Locate every Plasmodium falciparum-infected red blood cell.
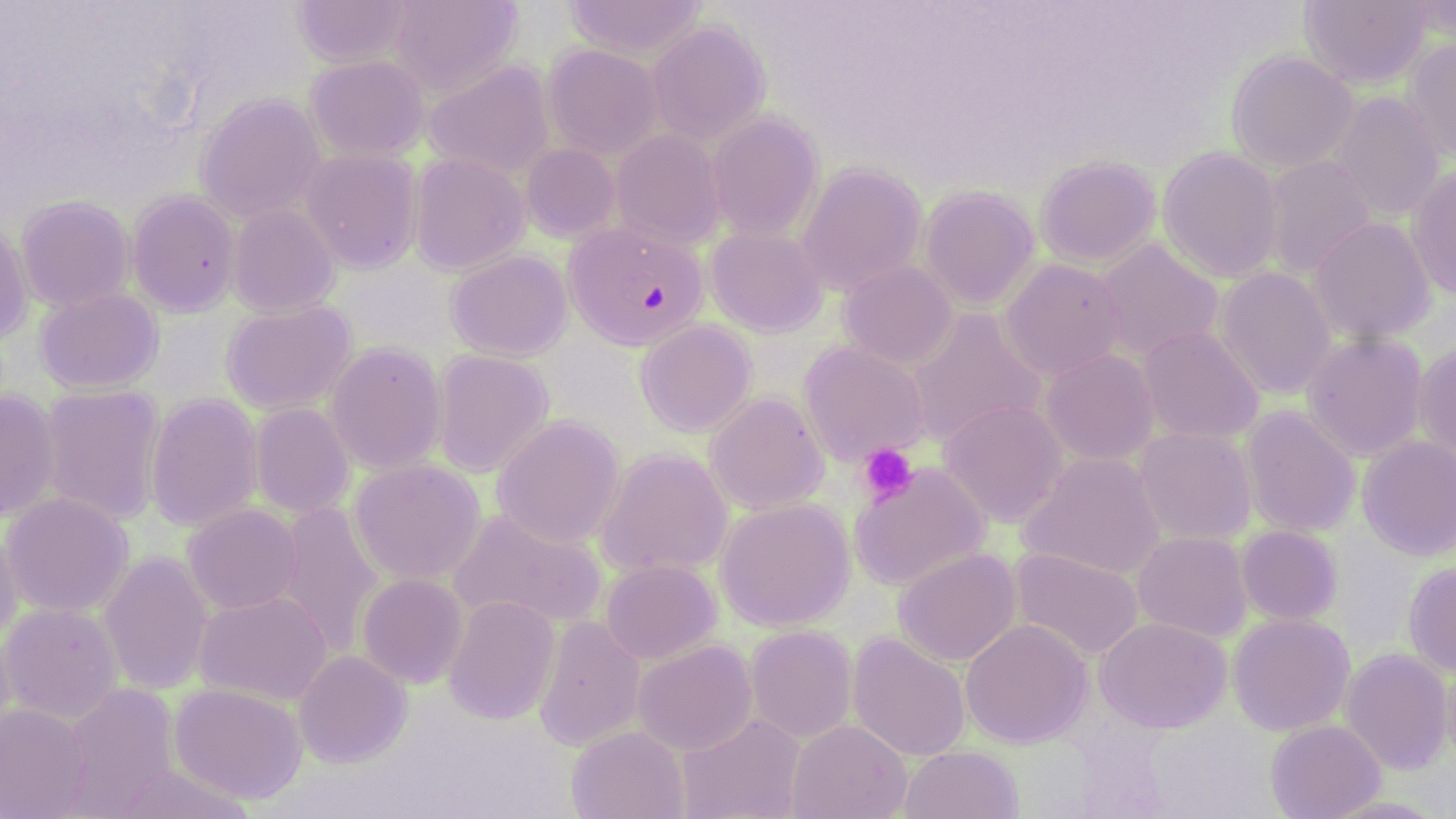
Approximate bounding boxes as (x1,y1)-(x2,y2) corner pairs in pixels.
Plasmodium falciparum-infected red blood cells: (564,221)-(708,350).

Summary:
  - Uninfected red blood cell locations: (387,0)-(522,96), (564,0)-(707,60), (1299,0)-(1430,89), (292,1)-(416,67), (1403,1)-(1455,41), (647,20)-(770,146), (1404,36)-(1456,162), (542,44)-(663,160), (1226,51)-(1358,171), (305,55)-(430,161), (423,61)-(556,181), (1329,91)-(1444,222), (195,93)-(325,223), (707,112)-(823,242), (611,130)-(726,249), (521,143)-(620,242), (1157,146)-(1283,283), (301,149)-(423,273), (410,153)-(529,275), (1262,155)-(1376,278), (1034,156)-(1161,268), (796,163)-(927,295), (1407,166)-(1456,299), (919,186)-(1039,310), (127,191)-(241,316), (16,195)-(135,311), (228,204)-(340,318), (1308,216)-(1436,344), (0,221)-(33,345), (705,226)-(828,337), (1094,239)-(1224,361), (446,249)-(572,360), (999,258)-(1127,382), (838,261)-(958,369), (1215,267)-(1336,400), (35,288)-(163,394), (220,301)-(356,414), (906,308)-(1047,447), (635,319)-(757,437), (1137,325)-(1264,444), (1302,332)-(1428,461), (325,342)-(447,475), (799,342)-(931,466), (1413,342)-(1456,467), (432,349)-(554,478), (1041,349)-(1159,465), (40,384)-(166,525), (0,389)-(61,523), (145,393)-(263,532), (705,393)-(829,514), (938,400)-(1068,527), (250,403)-(354,519), (1240,406)-(1360,537), (492,415)-(625,548), (1134,427)-(1256,545), (1356,435)-(1456,561), (596,447)-(733,578), (1019,452)-(1166,580), (348,459)-(486,584), (849,462)-(990,591), (1,492)-(135,618), (715,498)-(855,631), (275,501)-(384,656), (182,504)-(302,614), (447,509)-(608,632), (0,523)-(21,643), (1237,525)-(1343,625), (1133,531)-(1252,641), (1009,547)-(1143,660), (894,548)-(1021,666), (99,551)-(213,696), (600,559)-(721,664), (1403,562)-(1456,676), (357,573)-(468,688), (193,591)-(332,706), (443,595)-(560,725), (0,603)-(124,724), (1227,613)-(1355,736), (533,615)-(646,750), (1095,617)-(1232,733), (960,619)-(1092,748), (745,625)-(857,744), (0,626)-(17,750), (848,632)-(970,762), (632,640)-(757,756), (1340,648)-(1454,775), (293,650)-(412,768), (1440,659)-(1456,771), (60,683)-(180,816), (169,683)-(308,804), (0,703)-(92,818), (676,712)-(806,819), (786,719)-(911,819), (1265,719)-(1385,819), (565,725)-(689,819), (899,745)-(1024,819), (113,763)-(256,819), (1320,795)-(1450,819)
  - Platelet locations: (857,443)-(919,505)
  - Slide-level diagnosis: Plasmodium falciparum
  - Image size: 1456×819 pixels
  - Modality: light microscopy
  - Preparation: thin blood film
  - Stain: May-Grünwald-Giemsa
  - Field of view: one of a larger specimen
  - Magnification: 1000x